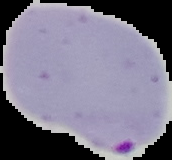

image_size: 172×160 pixels
image_type: segmented cell region with the area outside set to black
preparation: thin blood film
malaria_status: parasitized